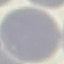

Result: negative for malaria parasites. Automatically extracted cell patch, resized to 64 × 64 pixels. Photographed with a smartphone camera at the microscope eyepiece. Thin smear of blood. Giemsa-stained preparation.